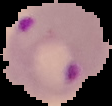
Summary:
  - Result: malaria parasites detected
  - Image size: 112×106 pixels
  - Image type: segmented cell region on a black background
  - Preparation: thin blood film